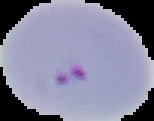
Segmented cell region on a black background. Result: Plasmodium parasites identified. From a thin blood smear. Image is 154×121 pixels.